Locate every leukocyte (white blood cell).
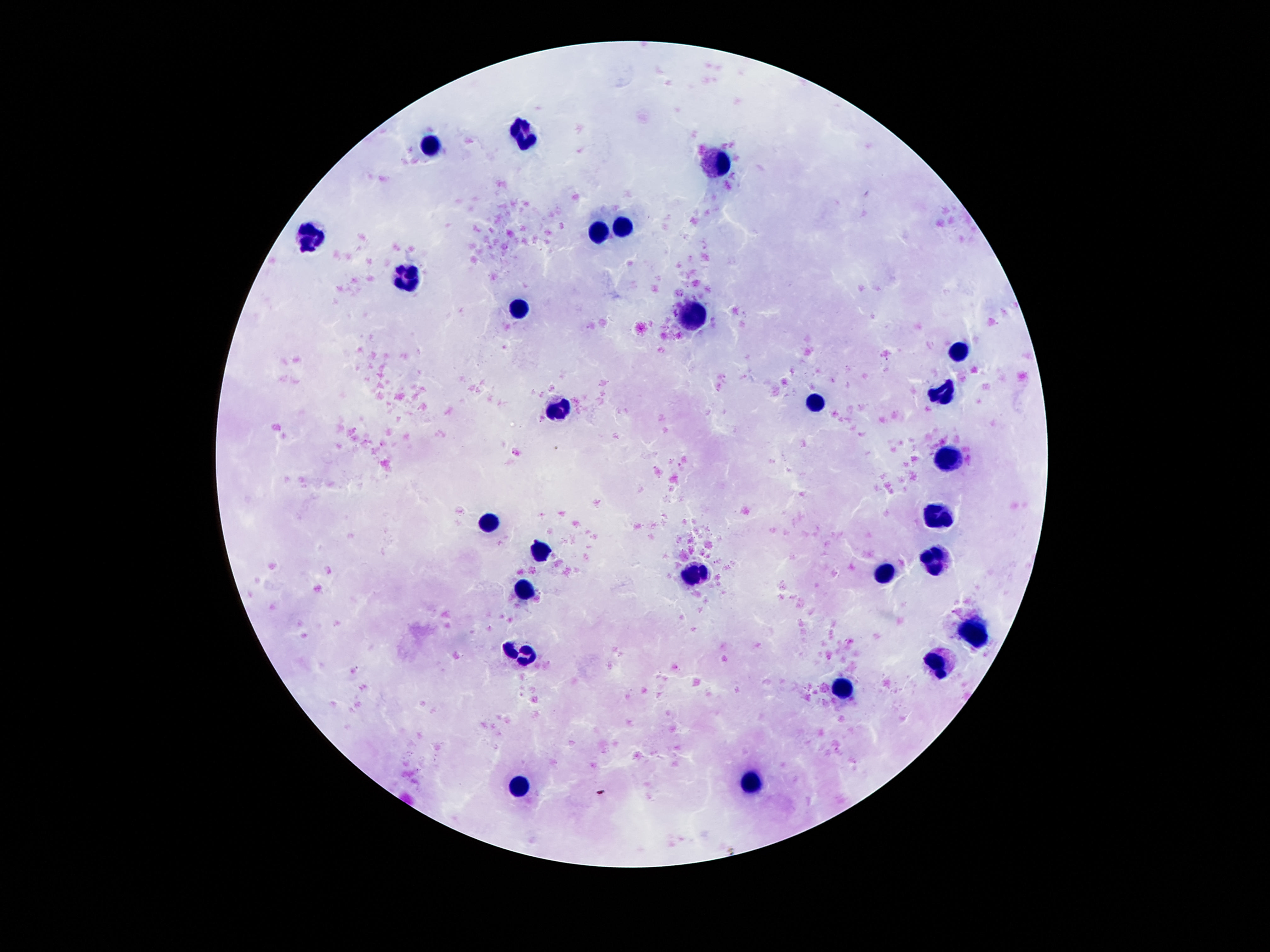

Approximate centers as (x, y) in pixels.
Leukocytes: (528, 134), (430, 145), (714, 162), (626, 226), (602, 229), (308, 238), (409, 276), (518, 309), (693, 313), (957, 353), (943, 390), (815, 401), (556, 409), (950, 458), (938, 518), (488, 521), (542, 551), (934, 558), (698, 575), (880, 575), (528, 589), (976, 633), (941, 666), (843, 687), (752, 785), (516, 791).

Photographed through the microscope eyepiece with a smartphone camera. Thick blood film. Patient malaria status: negative. 100x magnification. Image is 1270×952 pixels. Giemsa stain. One field from this slide.